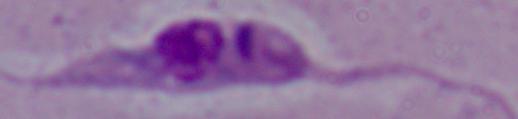
Summary:
  - Identification: Leishmania
  - Modality: micrograph
  - Magnification: 1000x